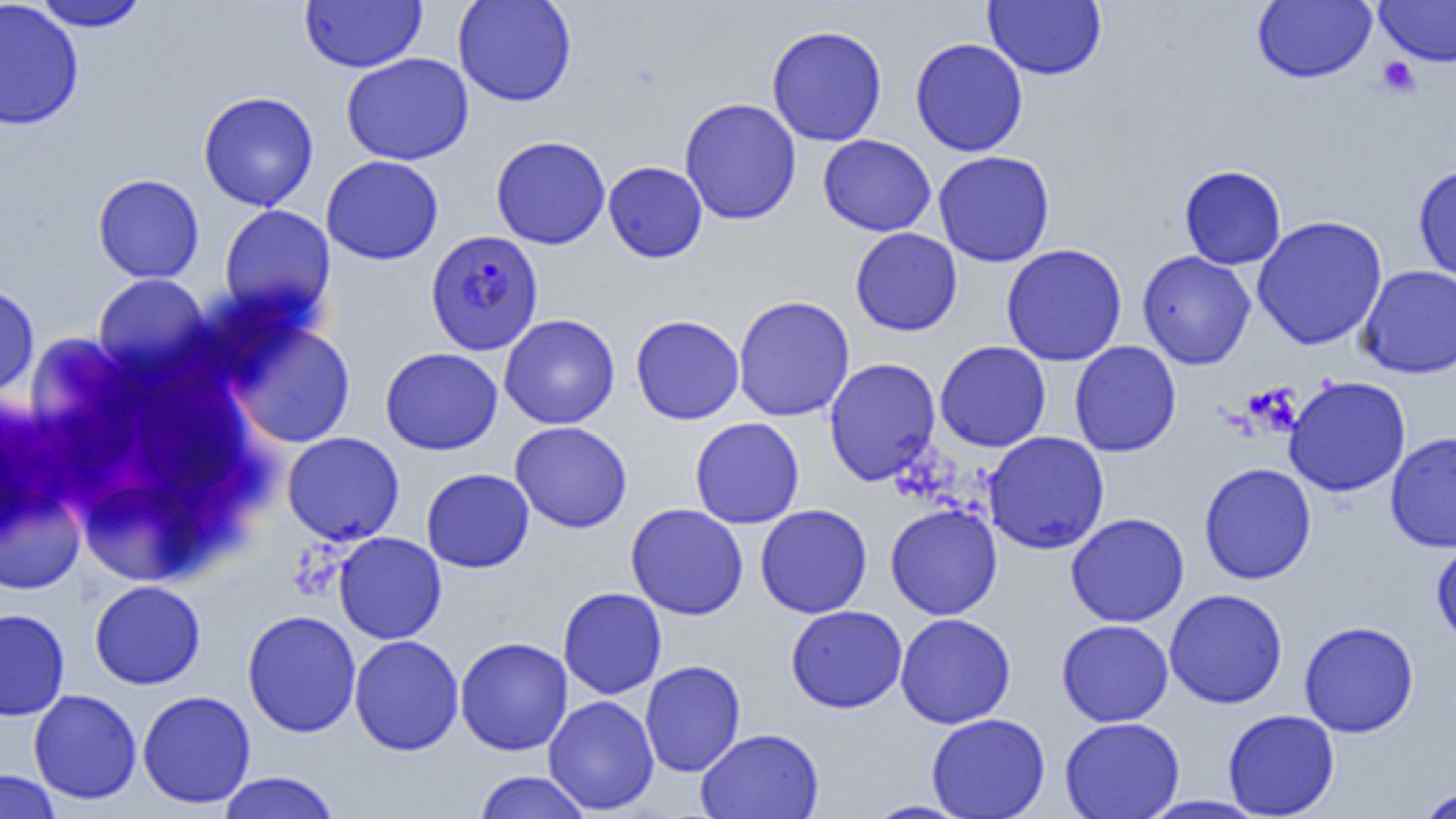 Approximate bounding boxes as (x1,y1)-(x2,y2) corner pairs in pixels. Plasmodium falciparum-infected red blood cell locations: (425,229)-(544,355). Uninfected red blood cell locations: (452,0)-(578,107), (983,0)-(1107,80), (1251,0)-(1376,84), (0,1)-(84,131), (31,1)-(149,32), (300,1)-(427,72), (1375,1)-(1456,67), (766,24)-(888,146), (910,38)-(1028,157), (340,52)-(474,166), (198,91)-(318,211), (679,97)-(802,225), (818,134)-(936,237), (491,135)-(610,249), (933,150)-(1055,267), (320,154)-(444,265), (603,161)-(708,263), (1178,164)-(1287,270), (1413,164)-(1456,283), (92,173)-(205,283), (218,204)-(336,321), (1251,215)-(1388,351), (850,227)-(962,336), (1001,243)-(1128,366), (1137,250)-(1256,370), (1357,265)-(1456,378), (93,273)-(210,376), (0,284)-(39,400), (732,295)-(855,422), (499,314)-(621,429), (630,314)-(745,425), (228,320)-(356,449), (25,333)-(141,474), (934,340)-(1052,452), (1069,340)-(1181,458), (380,347)-(503,455), (823,357)-(941,487), (138,365)-(251,495), (1284,376)-(1411,497), (689,417)-(805,529), (510,421)-(633,533), (1385,430)-(1456,553), (282,431)-(404,546), (983,431)-(1110,555), (1198,462)-(1317,584), (421,468)-(534,573), (0,484)-(86,595), (80,487)-(206,584), (626,503)-(749,620), (755,503)-(873,619), (885,503)-(1002,620), (1065,512)-(1189,627), (334,532)-(446,644), (1431,538)-(1456,649), (89,580)-(206,689), (558,587)-(667,699), (1164,588)-(1288,709), (786,605)-(907,713), (0,608)-(70,721), (242,610)-(361,737), (895,613)-(1016,729), (1057,619)-(1174,727), (1299,621)-(1420,737), (349,634)-(464,756), (455,636)-(573,756), (640,660)-(746,777), (28,689)-(142,805), (137,690)-(256,809), (543,695)-(659,814), (1222,709)-(1340,818), (926,712)-(1051,819), (1059,716)-(1185,819), (695,728)-(824,819), (0,769)-(63,819), (473,770)-(592,819), (216,771)-(341,819), (1417,785)-(1456,819), (1139,795)-(1270,818), (863,799)-(974,819). Platelet locations: (1377,57)-(1421,99). Slide-level diagnosis: Plasmodium falciparum. Image is 1456×819 pixels. Light microscopy. Captured at 1000x magnification. Thin blood film. One field of a larger specimen.